Outline each blood parasite and name the species.
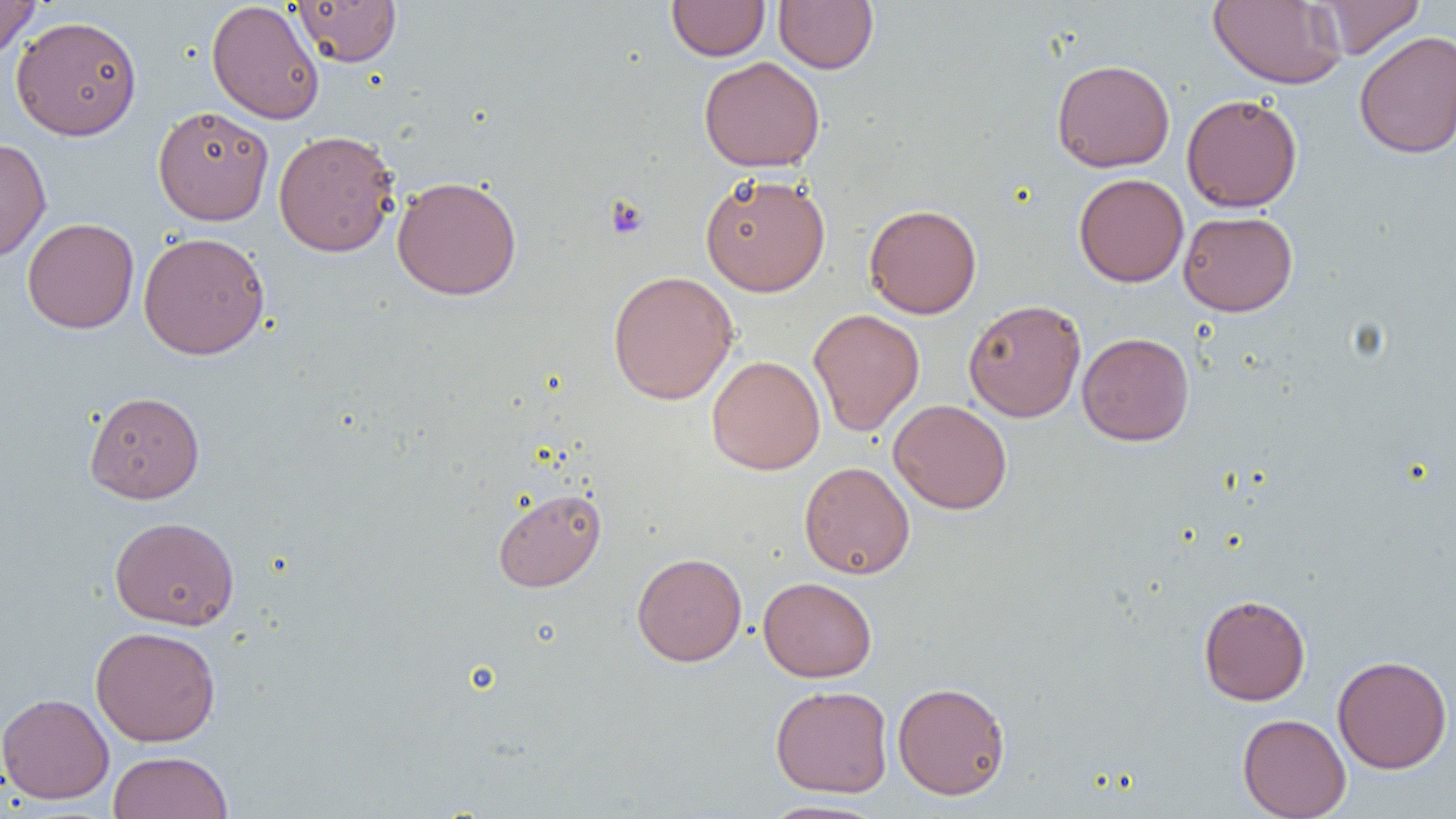
No blood parasites observed.

Approximate bounding boxes as (x1,y1)-(x2,y2) corner pairs in pixels. Platelet locations: (606,196)-(649,240). Uninfected red blood cell locations: (0,0)-(41,61), (292,0)-(402,67), (774,0)-(877,73), (1209,0)-(1346,89), (1311,0)-(1425,59), (206,1)-(324,125), (667,1)-(770,61), (11,15)-(143,141), (1354,31)-(1456,158), (699,56)-(825,172), (1051,59)-(1175,172), (1181,93)-(1303,212), (153,105)-(274,225), (273,129)-(399,257), (0,138)-(51,261), (700,173)-(831,296), (1074,173)-(1189,287), (392,175)-(522,301), (864,204)-(982,319), (1178,210)-(1298,316), (22,217)-(139,333), (138,231)-(269,360), (607,270)-(738,405), (963,299)-(1087,422), (808,308)-(925,436), (1077,332)-(1194,446), (706,355)-(825,475), (85,390)-(205,504), (889,399)-(1012,514), (799,461)-(915,579), (493,487)-(607,592), (110,516)-(239,630), (632,552)-(747,666), (758,577)-(877,682), (1198,594)-(1311,706), (90,625)-(221,746), (1332,655)-(1452,773), (892,681)-(1011,800), (770,685)-(893,798), (0,692)-(114,804), (1238,713)-(1351,819), (108,751)-(233,819), (759,800)-(888,819). Slide-level diagnosis: negative for blood parasites. Optical microscopy. One field of a larger specimen. Image is 1456×819 pixels. Captured at 1000x magnification. Thin blood film.